Describe the morphology of the red blood cells.
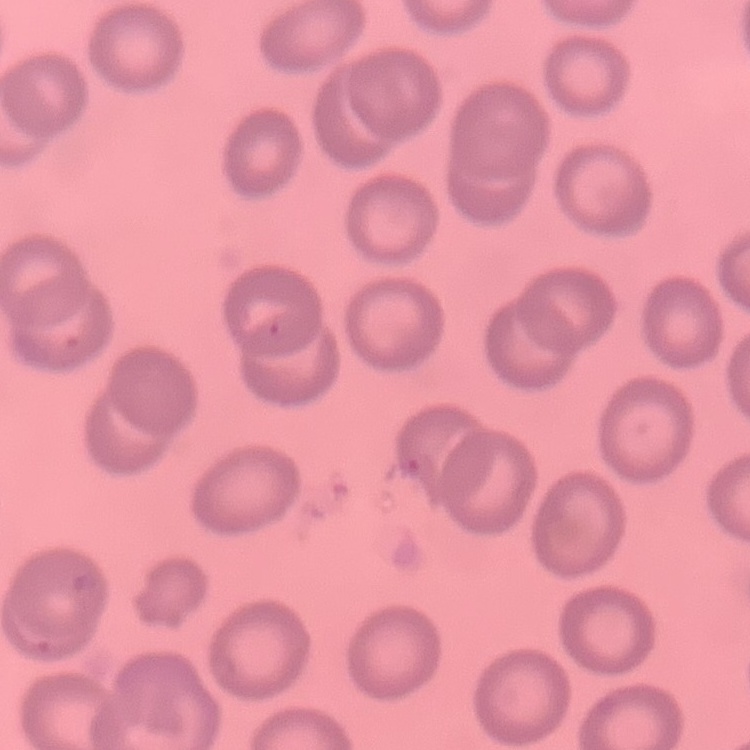
They show no rouleaux formation.

Summary:
  - Image type: one tile cut from a larger photomicrograph
  - Stain: Field's or Giemsa
  - Preparation: thin peripheral smear